Identify the parasite.
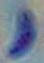
This is Toxoplasma gondii.

Micrograph. Captured at 1000x magnification.